State which parasite is depicted.
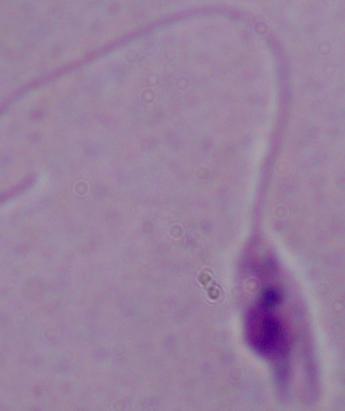

This is Leishmania.

Summary:
  - Magnification: 1000x
  - Modality: photomicrograph